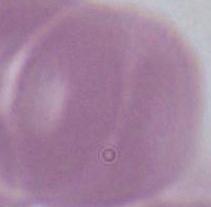
Summary:
  - Identification: red blood cell
  - Magnification: 1000x
  - Modality: micrograph